Report the malaria status of this cell.
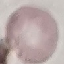
Uninfected.

Summary:
  - Stain: Giemsa
  - Preparation: thin blood film
  - Capture: smartphone camera at the microscope eyepiece
  - Image type: automatically extracted cell patch, resized to 64 × 64 pixels